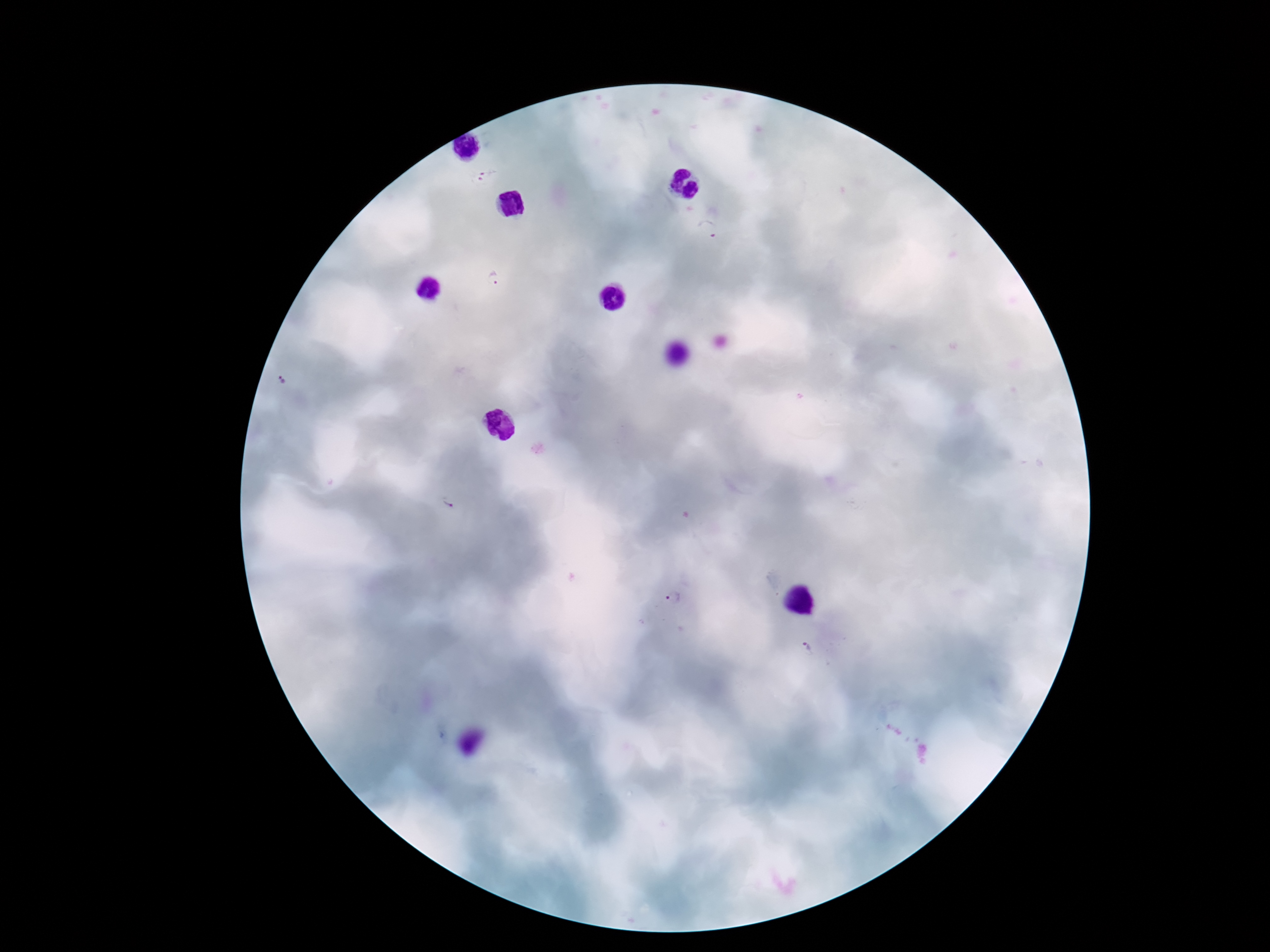
Approximate object centers, in pixels from the top-left corner.
Summary:
  - Plasmodium parasite locations: (x=485, y=173), (x=708, y=227), (x=493, y=278), (x=284, y=382), (x=449, y=506), (x=672, y=601), (x=806, y=647)
  - Patient malaria status: positive
  - Image size: 1270×952 pixels
  - Field of view: single
  - Preparation: thick blood film
  - Capture: smartphone camera through the microscope eyepiece
  - Stain: Giemsa
  - Magnification: 100x